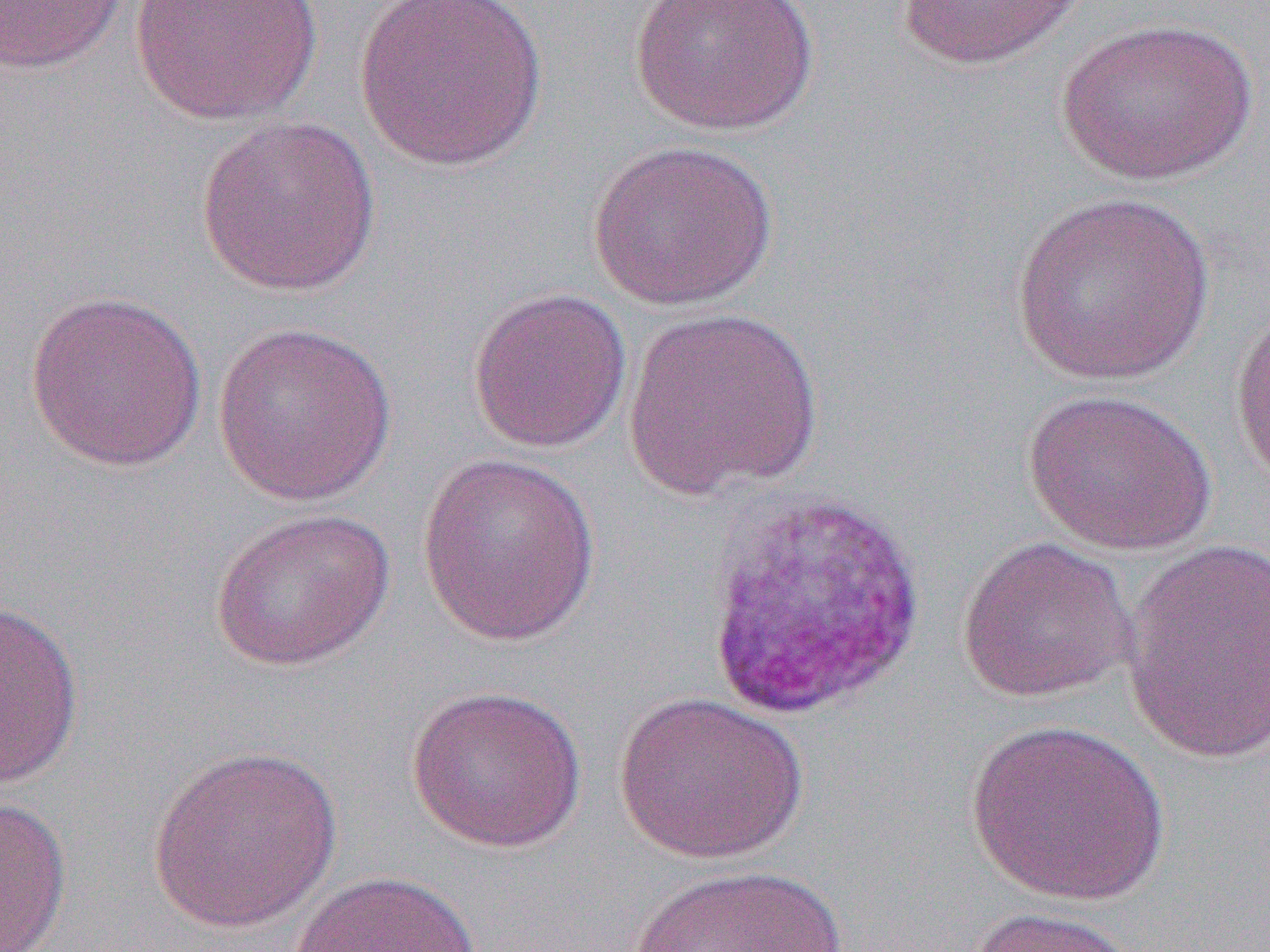 Approximate bounding boxes as named x1/y1/x2/y2 corners in pixels. Uninfected red blood cell locations: (x1=0, y1=0, x2=129, y2=75), (x1=129, y1=0, x2=323, y2=126), (x1=350, y1=0, x2=551, y2=173), (x1=628, y1=0, x2=820, y2=137), (x1=896, y1=0, x2=1090, y2=70), (x1=1053, y1=16, x2=1260, y2=186), (x1=195, y1=115, x2=382, y2=297), (x1=586, y1=138, x2=779, y2=311), (x1=1010, y1=192, x2=1217, y2=387), (x1=467, y1=287, x2=633, y2=454), (x1=24, y1=289, x2=208, y2=472), (x1=1230, y1=298, x2=1270, y2=491), (x1=622, y1=305, x2=824, y2=499), (x1=212, y1=320, x2=398, y2=507), (x1=1020, y1=387, x2=1218, y2=557), (x1=416, y1=452, x2=601, y2=646), (x1=208, y1=506, x2=396, y2=672), (x1=956, y1=535, x2=1138, y2=703), (x1=1122, y1=539, x2=1269, y2=765), (x1=0, y1=600, x2=85, y2=790), (x1=406, y1=683, x2=587, y2=853), (x1=613, y1=691, x2=809, y2=864), (x1=966, y1=720, x2=1172, y2=906), (x1=147, y1=744, x2=343, y2=933), (x1=0, y1=796, x2=71, y2=952), (x1=627, y1=861, x2=856, y2=952), (x1=288, y1=869, x2=482, y2=951), (x1=964, y1=906, x2=1142, y2=952). Slide-level diagnosis: Plasmodium vivax. Image is 1270×952 pixels. Thin blood film. Light microscopy. 1000x magnification. One field of a larger specimen.